Classify this cell by malaria status.
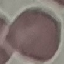

Uninfected.

Thin blood film. Photographed with a smartphone camera at the microscope eyepiece. Automatically extracted cell patch, resized to 64 × 64 pixels. Giemsa-stained preparation.